Give the position of every Plasmodium parasite visible.
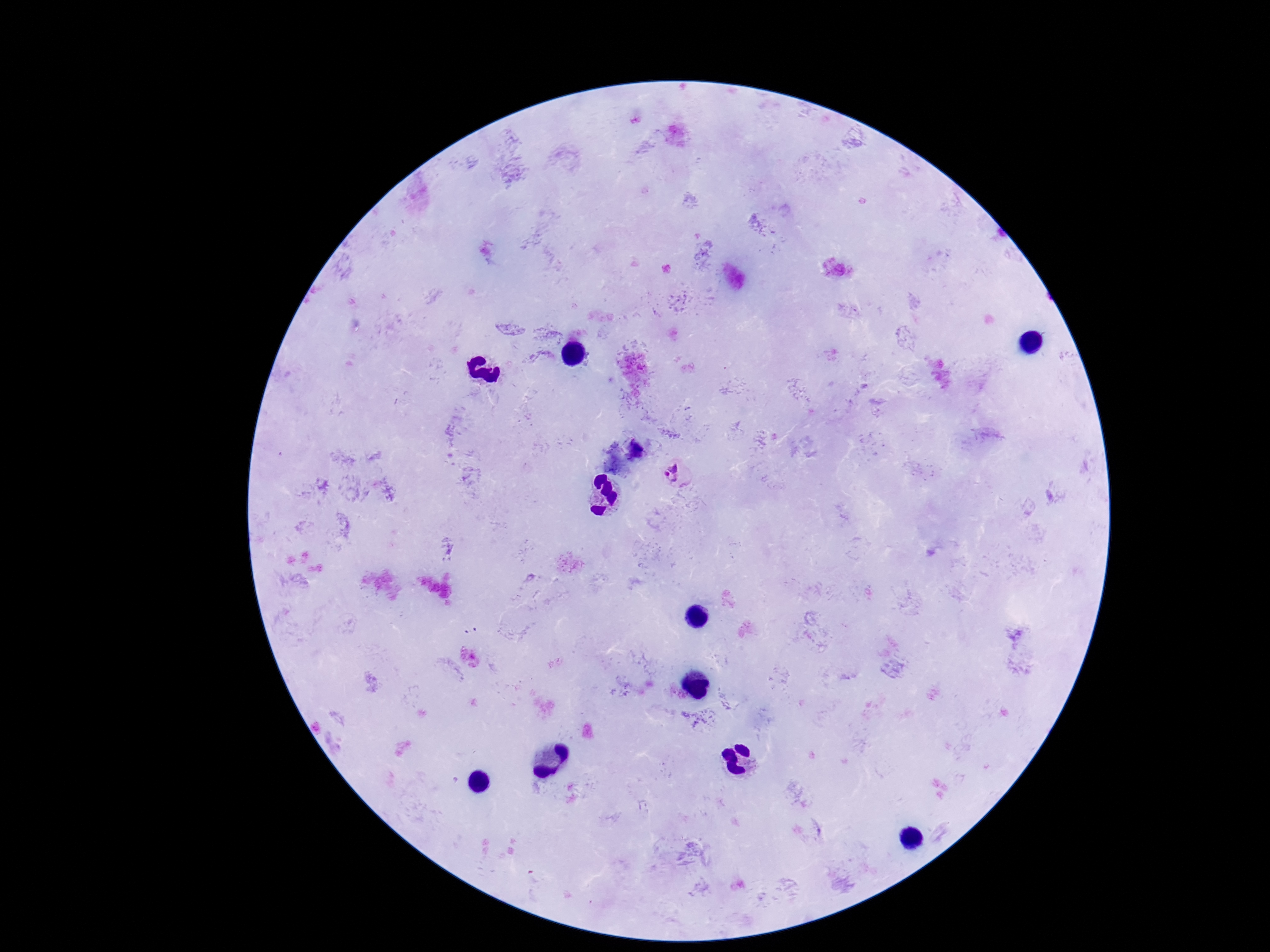

Approximate object centers, in pixels from the top-left corner.
Plasmodium parasites: (x=677, y=475).

{
  "image_size": "1270×952 pixels",
  "stain": "Giemsa",
  "patient_malaria_status": "positive",
  "magnification": "100x",
  "field_of_view": "one from this slide",
  "preparation": "thick peripheral-blood smear",
  "capture": "smartphone camera through the microscope eyepiece"
}